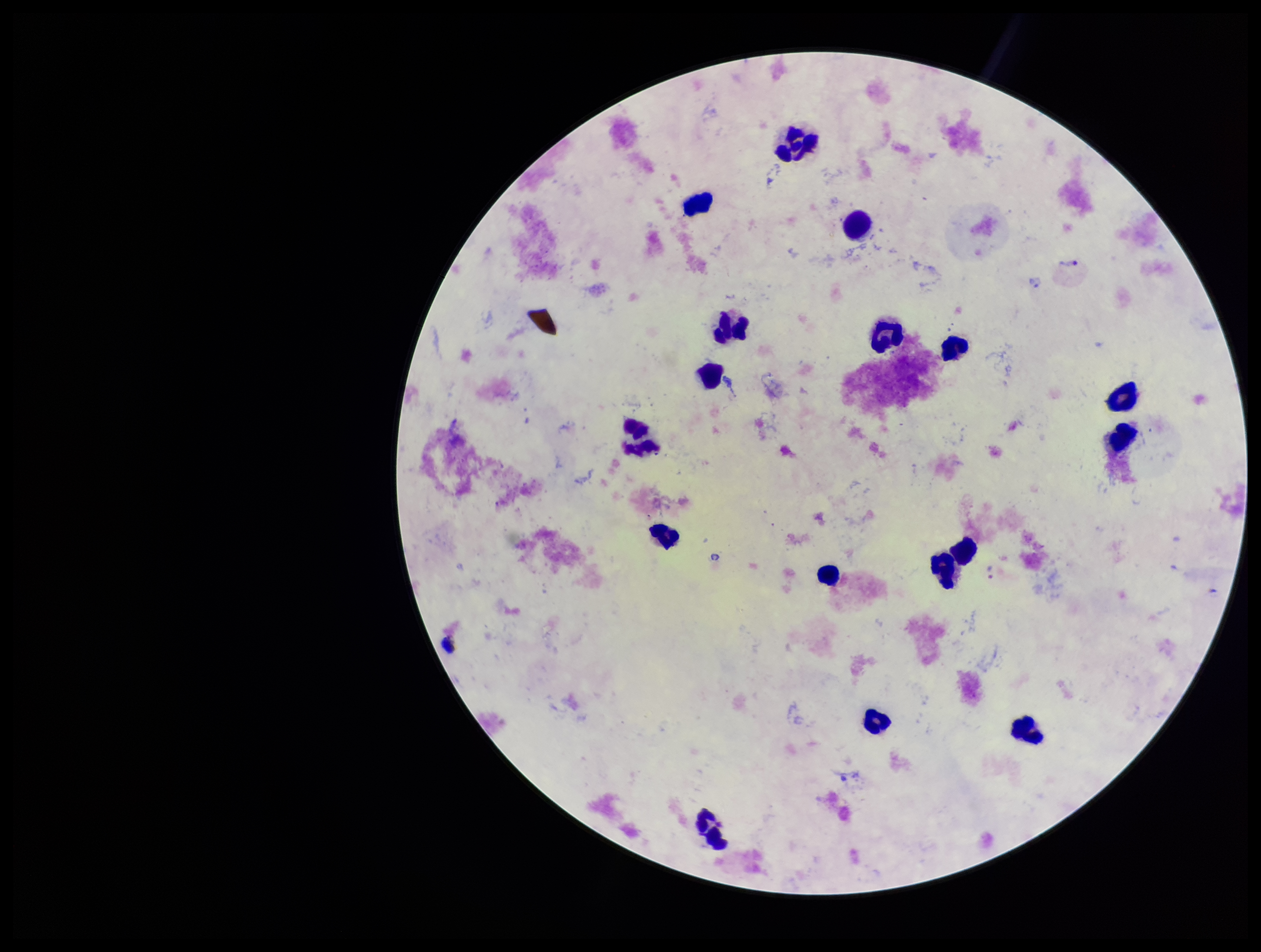

{
  "preparation": "thick blood smear",
  "field_of_view": "one from this slide",
  "leukocyte_count": 17,
  "image_size": "1261×952 pixels",
  "stain": "Giemsa",
  "parasite_count": 2,
  "species_reported_for_this_patient": "Plasmodium vivax",
  "capture": "smartphone photograph through the microscope eyepiece",
  "patient_malaria_status": "positive",
  "plasmodium_parasites": "identified"
}